Report the malaria status of this cell.
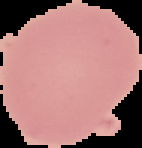
It is uninfected.

From a thin blood film. Segmented cell region on a black background. Image is 142×148 pixels.